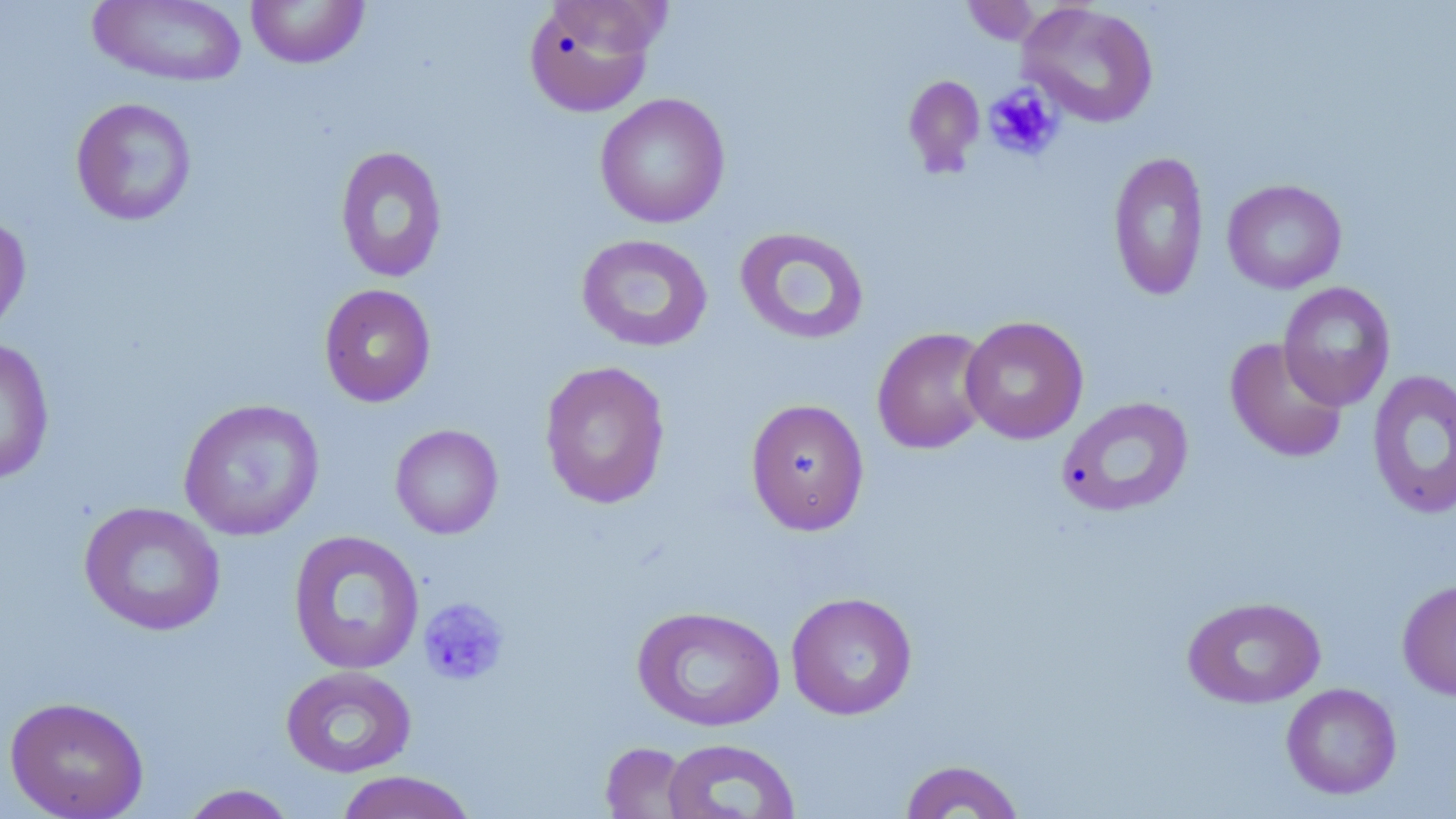
{
  "slide_level_diagnosis": "no evidence of blood parasites",
  "uninfected_red_blood_cell_locations": "approximate bounding boxes as (x1, y1, x2, y2) in pixels: (88, 0, 247, 87), (245, 0, 370, 69), (522, 1, 663, 117), (960, 1, 1047, 46), (1017, 2, 1159, 128), (902, 74, 985, 179), (595, 93, 730, 229), (70, 97, 198, 226), (334, 146, 449, 283), (1108, 150, 1209, 302), (1222, 179, 1347, 294), (0, 211, 32, 341), (734, 226, 869, 345), (576, 233, 713, 353), (1278, 281, 1396, 411), (318, 284, 436, 407), (960, 315, 1089, 444), (872, 326, 994, 454), (0, 337, 55, 485), (1224, 337, 1349, 463), (539, 360, 671, 509), (1367, 368, 1456, 520), (1056, 396, 1194, 518), (177, 398, 325, 541), (745, 398, 870, 535), (390, 424, 504, 539), (78, 501, 226, 636), (287, 530, 425, 675), (1397, 579, 1456, 701), (785, 592, 918, 720), (1182, 596, 1326, 708), (631, 605, 785, 732), (280, 665, 417, 778), (1281, 683, 1402, 800), (4, 695, 149, 819), (661, 738, 800, 819), (600, 742, 695, 818), (898, 759, 1026, 818), (334, 770, 478, 819), (178, 784, 299, 818)",
  "magnification": "1000x",
  "preparation": "thin blood film",
  "modality": "optical microscopy",
  "field_of_view": "one of a larger specimen",
  "stain": "May-Grünwald-Giemsa",
  "platelet_locations": "approximate bounding boxes as (x1, y1, x2, y2) in pixels: (983, 84, 1063, 161), (418, 596, 511, 687)",
  "image_size": "1456×819 pixels"
}